Describe the morphology of the red blood cells.
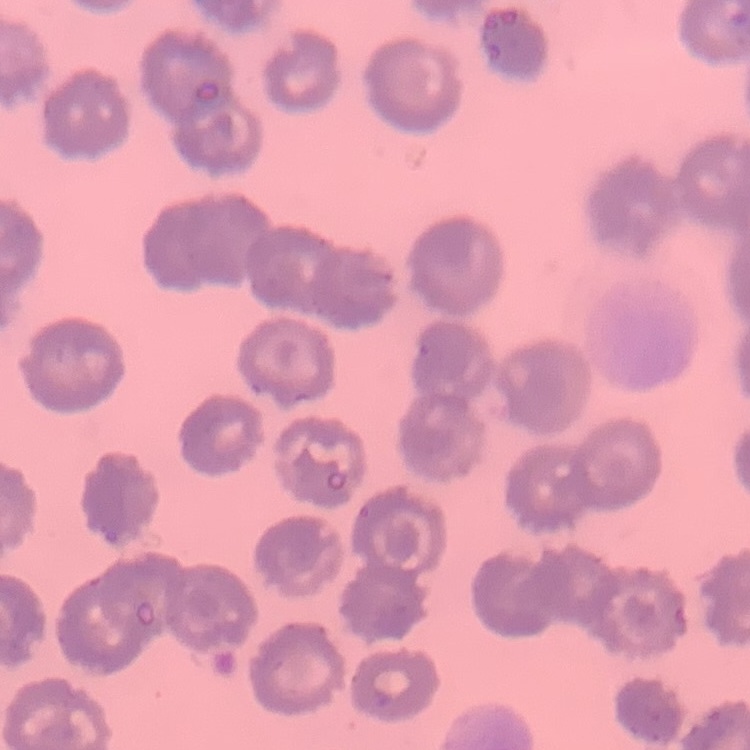
They show no rouleaux formation.

Summary:
  - Preparation: thin blood smear
  - Stain: Field's or Giemsa
  - Image type: square crop of a larger photomicrograph